Identify the parasite.
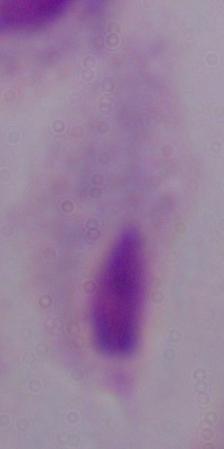
This is a trichomonad.

magnification: 1000x
modality: photomicrograph